Report the malaria status of this cell.
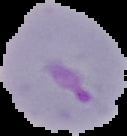
Parasitized.

From a thin blood film. Image is 127×136 pixels. Cell region segmented out of the field of view; the surrounding area is masked to black.